Name the cell type shown.
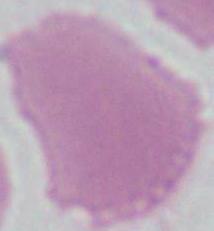
An erythrocyte.

Summary:
  - Modality: micrograph
  - Magnification: 1000x